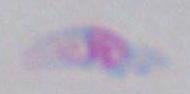
{
  "modality": "photomicrograph",
  "identification": "Toxoplasma gondii",
  "magnification": "1000x"
}